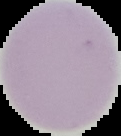
image type = segmented cell region on a black background
preparation = thin blood film
malaria status = uninfected
image size = 121×136 pixels